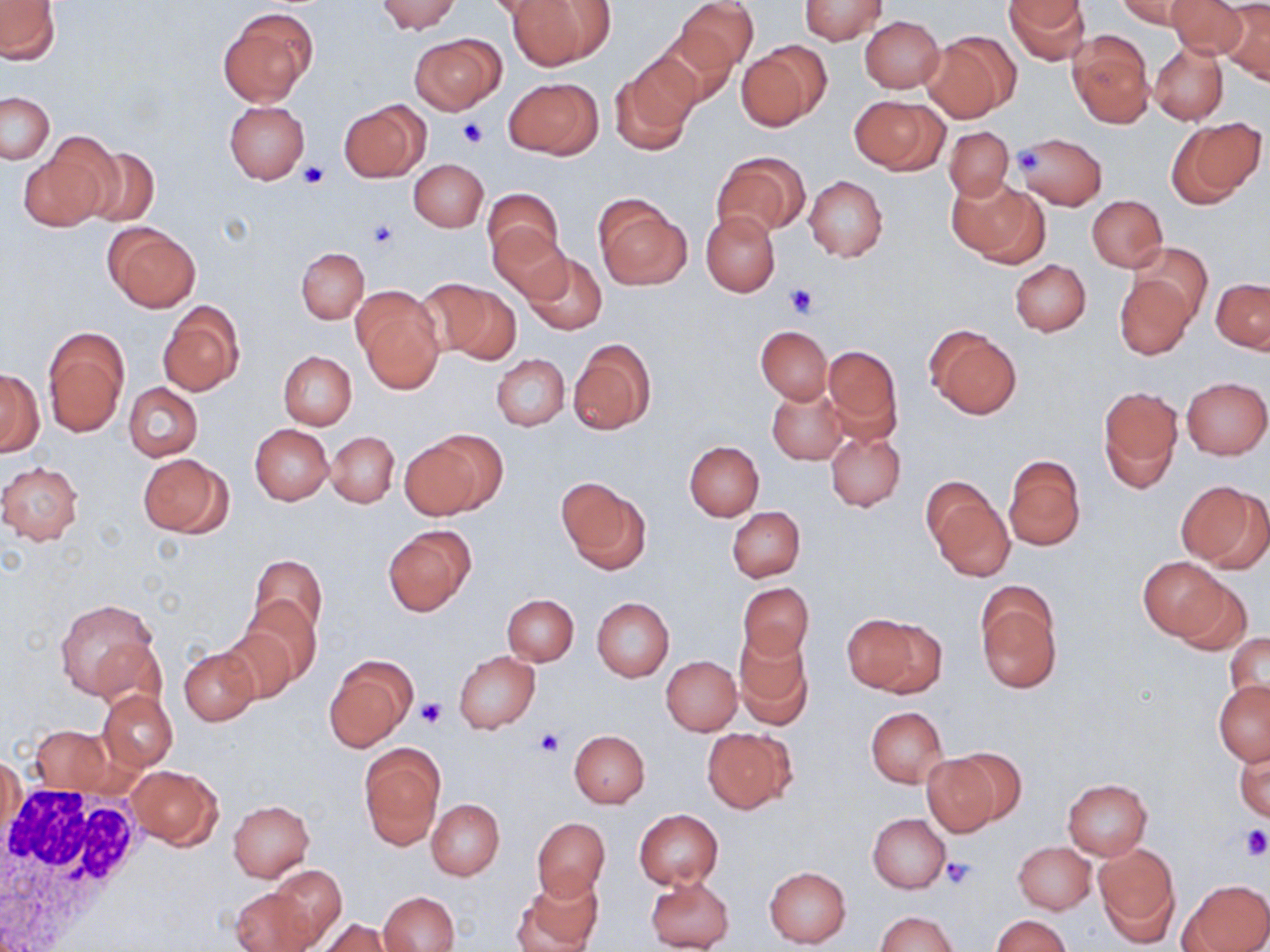 Approximate bounding boxes as named x1/y1/x2/y2 corners in pixels. White blood cell locations: (x1=0, y1=780, x2=147, y2=944). Platelet locations: (x1=457, y1=118, x2=490, y2=146), (x1=1009, y1=147, x2=1047, y2=178), (x1=299, y1=160, x2=330, y2=188), (x1=366, y1=221, x2=399, y2=251), (x1=784, y1=284, x2=816, y2=317), (x1=414, y1=696, x2=446, y2=727), (x1=535, y1=728, x2=564, y2=756), (x1=1241, y1=827, x2=1270, y2=860), (x1=942, y1=856, x2=976, y2=889). Uninfected red blood cell locations: (x1=376, y1=0, x2=460, y2=33), (x1=509, y1=0, x2=612, y2=69), (x1=677, y1=0, x2=757, y2=75), (x1=799, y1=0, x2=887, y2=45), (x1=1006, y1=0, x2=1088, y2=65), (x1=1166, y1=0, x2=1249, y2=59), (x1=1119, y1=1, x2=1199, y2=29), (x1=0, y1=2, x2=60, y2=62), (x1=1222, y1=2, x2=1270, y2=85), (x1=217, y1=6, x2=316, y2=107), (x1=859, y1=15, x2=944, y2=93), (x1=651, y1=29, x2=735, y2=110), (x1=1067, y1=30, x2=1154, y2=128), (x1=411, y1=32, x2=504, y2=115), (x1=922, y1=33, x2=1016, y2=122), (x1=736, y1=43, x2=827, y2=131), (x1=1149, y1=43, x2=1227, y2=124), (x1=608, y1=56, x2=697, y2=154), (x1=505, y1=76, x2=602, y2=159), (x1=1, y1=92, x2=54, y2=163), (x1=851, y1=94, x2=945, y2=174), (x1=224, y1=100, x2=310, y2=184), (x1=339, y1=103, x2=425, y2=182), (x1=1168, y1=118, x2=1264, y2=206), (x1=945, y1=126, x2=1015, y2=202), (x1=21, y1=135, x2=119, y2=231), (x1=1017, y1=136, x2=1108, y2=207), (x1=80, y1=144, x2=161, y2=227), (x1=711, y1=154, x2=807, y2=239), (x1=410, y1=159, x2=487, y2=231), (x1=805, y1=175, x2=888, y2=262), (x1=952, y1=180, x2=1047, y2=265), (x1=483, y1=186, x2=563, y2=267), (x1=594, y1=194, x2=693, y2=290), (x1=1087, y1=196, x2=1167, y2=271), (x1=701, y1=211, x2=780, y2=296), (x1=104, y1=223, x2=200, y2=312), (x1=489, y1=223, x2=570, y2=303), (x1=1130, y1=242, x2=1212, y2=319), (x1=297, y1=248, x2=368, y2=323), (x1=521, y1=251, x2=607, y2=335), (x1=1010, y1=260, x2=1091, y2=336), (x1=1114, y1=273, x2=1194, y2=359), (x1=424, y1=277, x2=518, y2=362), (x1=1212, y1=279, x2=1269, y2=352), (x1=353, y1=289, x2=443, y2=391), (x1=158, y1=302, x2=244, y2=397), (x1=925, y1=323, x2=1022, y2=420), (x1=757, y1=326, x2=831, y2=403), (x1=43, y1=328, x2=128, y2=435), (x1=568, y1=339, x2=655, y2=434), (x1=822, y1=344, x2=902, y2=438), (x1=279, y1=351, x2=356, y2=429), (x1=492, y1=354, x2=569, y2=431), (x1=0, y1=368, x2=43, y2=456), (x1=1181, y1=377, x2=1270, y2=459), (x1=123, y1=383, x2=203, y2=461), (x1=767, y1=385, x2=846, y2=465), (x1=1098, y1=387, x2=1182, y2=491), (x1=250, y1=424, x2=332, y2=505), (x1=325, y1=430, x2=398, y2=508), (x1=826, y1=430, x2=905, y2=512), (x1=414, y1=431, x2=506, y2=517), (x1=685, y1=441, x2=764, y2=520), (x1=138, y1=453, x2=230, y2=537), (x1=1004, y1=454, x2=1085, y2=552), (x1=0, y1=461, x2=84, y2=545), (x1=557, y1=478, x2=650, y2=574), (x1=1178, y1=481, x2=1269, y2=571), (x1=928, y1=488, x2=1014, y2=580), (x1=727, y1=506, x2=805, y2=582), (x1=383, y1=526, x2=475, y2=615), (x1=248, y1=555, x2=326, y2=636), (x1=1138, y1=555, x2=1231, y2=641), (x1=1170, y1=576, x2=1251, y2=657), (x1=737, y1=581, x2=814, y2=662), (x1=975, y1=587, x2=1061, y2=692), (x1=503, y1=594, x2=579, y2=665), (x1=55, y1=596, x2=159, y2=700), (x1=240, y1=596, x2=322, y2=685), (x1=591, y1=597, x2=674, y2=682), (x1=842, y1=613, x2=944, y2=696), (x1=219, y1=627, x2=299, y2=704), (x1=734, y1=631, x2=814, y2=728), (x1=1224, y1=632, x2=1270, y2=708), (x1=179, y1=648, x2=258, y2=725), (x1=454, y1=651, x2=539, y2=734), (x1=325, y1=656, x2=417, y2=753), (x1=662, y1=656, x2=741, y2=735), (x1=1214, y1=679, x2=1270, y2=765), (x1=98, y1=690, x2=177, y2=771), (x1=866, y1=706, x2=947, y2=787), (x1=30, y1=725, x2=114, y2=793), (x1=702, y1=728, x2=795, y2=811), (x1=568, y1=729, x2=650, y2=807), (x1=359, y1=744, x2=444, y2=848), (x1=1235, y1=744, x2=1269, y2=822), (x1=2, y1=752, x2=25, y2=855), (x1=922, y1=752, x2=1009, y2=834), (x1=126, y1=764, x2=222, y2=848), (x1=1062, y1=779, x2=1152, y2=860), (x1=427, y1=799, x2=504, y2=879), (x1=228, y1=800, x2=315, y2=880), (x1=635, y1=809, x2=723, y2=888), (x1=867, y1=813, x2=950, y2=893), (x1=531, y1=817, x2=610, y2=899), (x1=1014, y1=841, x2=1096, y2=915), (x1=1095, y1=843, x2=1180, y2=944), (x1=268, y1=864, x2=347, y2=948), (x1=764, y1=866, x2=852, y2=947), (x1=514, y1=874, x2=603, y2=952), (x1=645, y1=875, x2=735, y2=952), (x1=1180, y1=879, x2=1268, y2=951), (x1=230, y1=887, x2=317, y2=952), (x1=377, y1=891, x2=459, y2=951), (x1=876, y1=911, x2=958, y2=952), (x1=992, y1=915, x2=1070, y2=952), (x1=317, y1=918, x2=395, y2=952). Slide-level diagnosis: no evidence of blood parasites. May-Grünwald-Giemsa-stained preparation. Image is 1270×952 pixels. Thin blood film. Light microscopy. Captured at 1000x magnification. One field of a larger specimen.